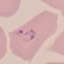
Result: malaria parasites detected. Acquired by smartphone through the microscope eyepiece. Cell patch, automatically extracted from a larger field of view and resized to 64 × 64 pixels. Giemsa-stained preparation. Thin blood film.